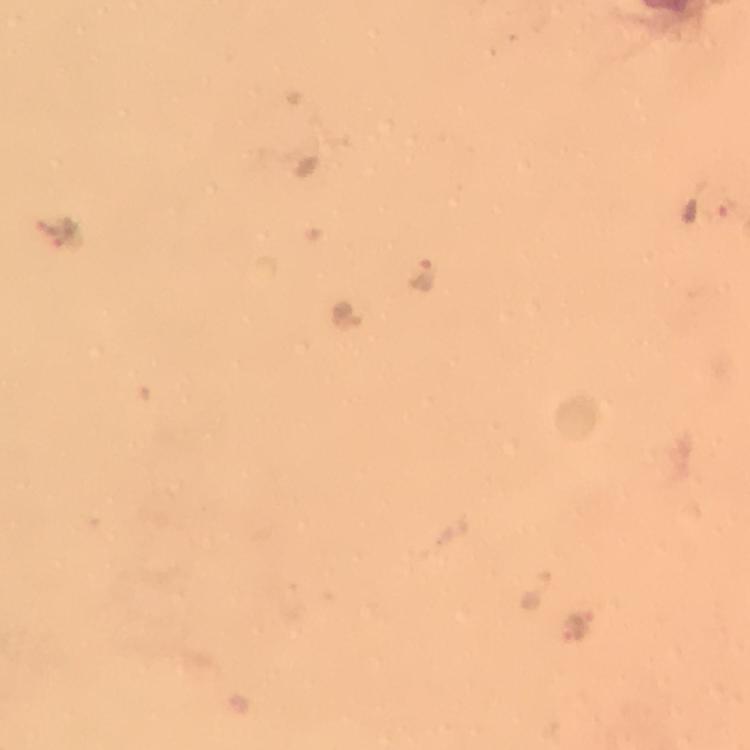

Approximate centers as [x, y] in pixels. Malaria parasite locations: [423, 275], [348, 315]. A crop from one field of view. Image is 750×750 pixels. Photographed through the microscope with a smartphone camera. Immersion oil was used. 100x magnification. From a malaria diagnostic workup. Thick smear. Giemsa-stained preparation.